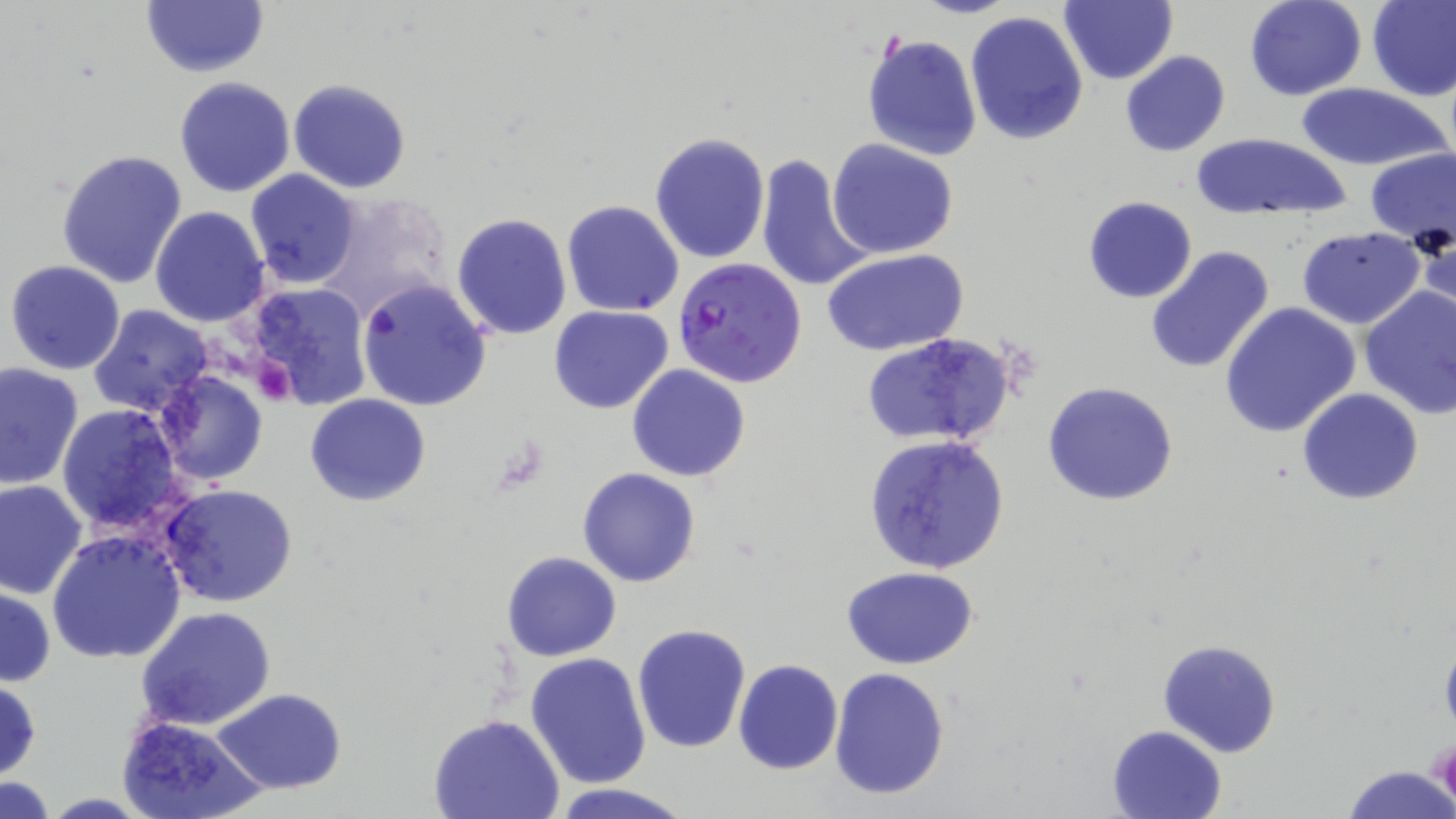

Approximate bounding boxes as [x1, y1, x2, y2] in pixels. Plasmodium falciparum-infected red blood cell locations: [674, 259, 808, 389]. Uninfected red blood cell locations: [1061, 0, 1178, 85], [1243, 0, 1367, 101], [1367, 0, 1456, 102], [140, 2, 268, 78], [964, 10, 1089, 145], [862, 33, 983, 161], [1120, 51, 1231, 157], [175, 76, 296, 198], [288, 78, 411, 195], [1294, 83, 1449, 170], [649, 131, 772, 265], [1189, 131, 1351, 222], [829, 139, 958, 258], [56, 148, 188, 290], [1362, 149, 1455, 239], [754, 154, 875, 293], [244, 169, 363, 290], [313, 193, 455, 319], [1083, 196, 1198, 303], [561, 200, 685, 317], [151, 206, 270, 329], [451, 211, 572, 339], [1413, 226, 1455, 325], [1297, 228, 1423, 328], [1144, 244, 1276, 375], [822, 249, 969, 356], [6, 259, 126, 375], [356, 280, 491, 411], [243, 283, 372, 408], [1359, 285, 1456, 418], [1220, 301, 1361, 437], [89, 306, 214, 416], [550, 306, 675, 414], [860, 332, 1016, 450], [0, 362, 83, 489], [626, 365, 750, 482], [153, 370, 269, 488], [1042, 381, 1178, 505], [1296, 388, 1424, 506], [305, 393, 431, 506], [56, 404, 186, 535], [862, 434, 1011, 576], [578, 467, 702, 586], [1, 480, 87, 600], [159, 484, 297, 606], [46, 529, 188, 665], [501, 551, 621, 661], [842, 567, 982, 670], [0, 586, 55, 686], [135, 606, 277, 731], [632, 623, 751, 754], [1158, 640, 1281, 758], [526, 652, 652, 789], [733, 658, 842, 776], [829, 668, 950, 800], [0, 676, 41, 780], [213, 688, 347, 793], [116, 713, 267, 819], [428, 714, 566, 819], [1106, 726, 1226, 819], [1342, 765, 1454, 819], [2, 776, 58, 817], [544, 782, 699, 818]. Platelet locations: [255, 358, 294, 405], [1432, 733, 1455, 806]. Slide-level diagnosis: Plasmodium falciparum. Thin blood smear. One field of a larger specimen. Captured at 1000x magnification. May-Grünwald-Giemsa stain. Image is 1456×819 pixels. Light microscopy.